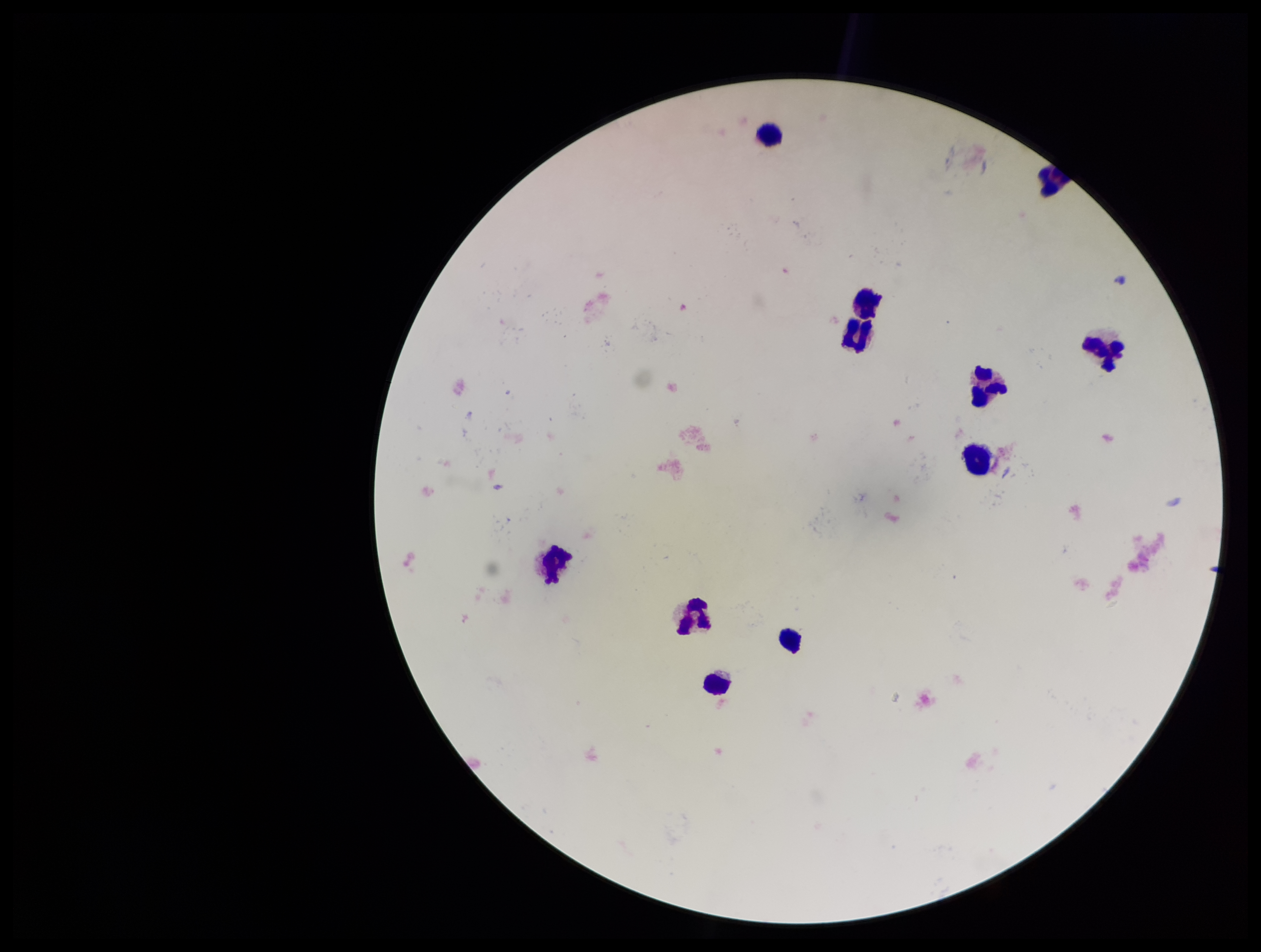
Summary:
  - Image size: 1261×952 pixels
  - Preparation: thick smear
  - Patient malaria status: negative
  - Field of view: single
  - Leukocyte count: 10
  - Capture: smartphone photograph through the microscope eyepiece
  - Parasite count: 0
  - Plasmodium parasites: none seen
  - Stain: Giemsa